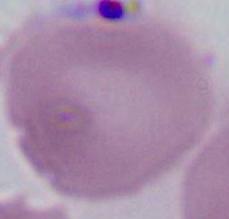

A red blood cell is seen. Micrograph. 1000x magnification.